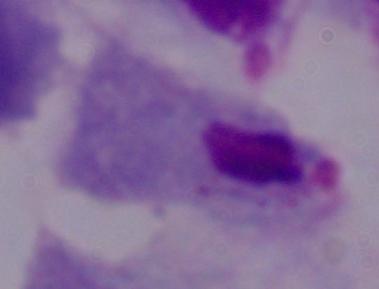 A trichomonad is shown. Captured at 1000x magnification. Photomicrograph.